Assess this cell for malaria.
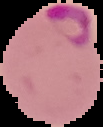
Parasitized.

image type = segmented cell region on a black background
image size = 103×127 pixels
preparation = thin blood smear